Name the parasite shown.
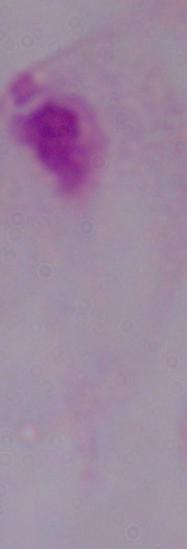
A trichomonad.

Photomicrograph. 1000x magnification.